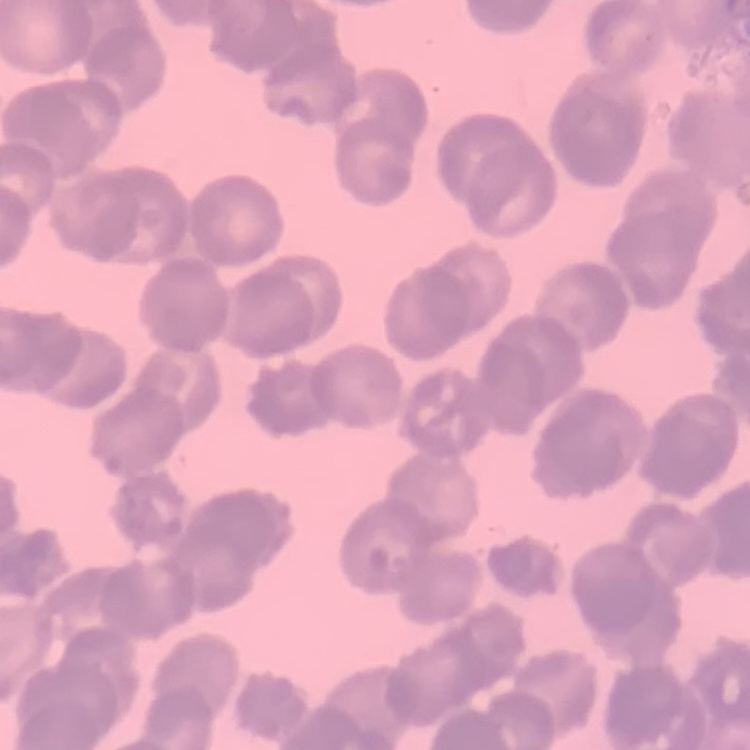
red blood cell morphology = rouleaux formation
preparation = thin blood film
stain = Field's or Giemsa
image type = square crop of a larger photomicrograph